Locate every malaria parasite.
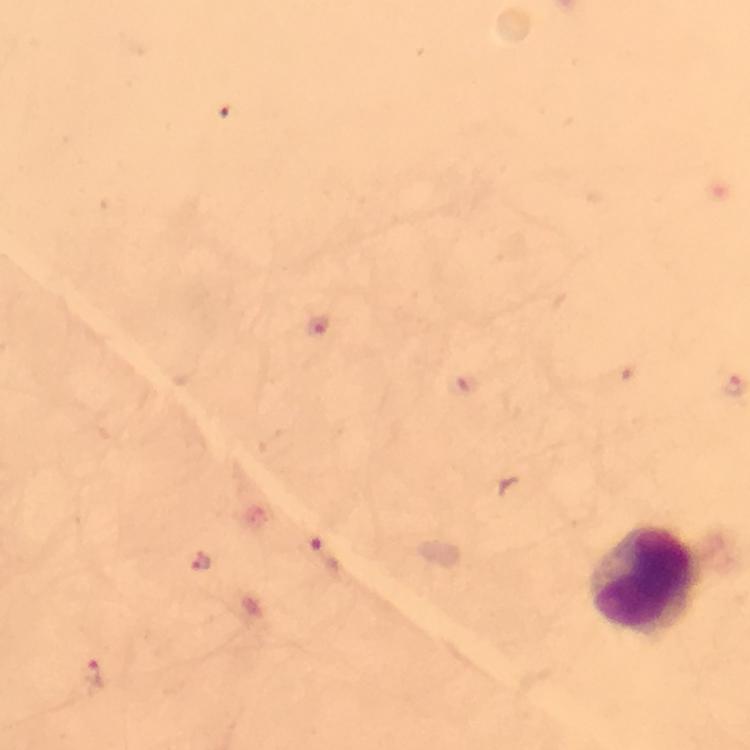
Approximate centers as [x, y] in pixels.
Malaria parasites: [318, 325], [323, 553], [199, 561], [93, 672].

capture = smartphone mounted on the microscope
context = from a diagnostic examination for malaria
image size = 750×750 pixels
preparation = thick blood film
leukocyte locations = approximate centers as [x, y] in pixels: [644, 579]
cropped from = a single field of view
immersion oil = used
stain = Giemsa
magnification = 100x